Classify this cell by malaria status.
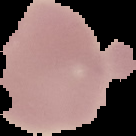
It is uninfected.

From a thin blood film. Image is 136×136 pixels. Segmented cell region on a black background.